Look for parasitized red blood cells.
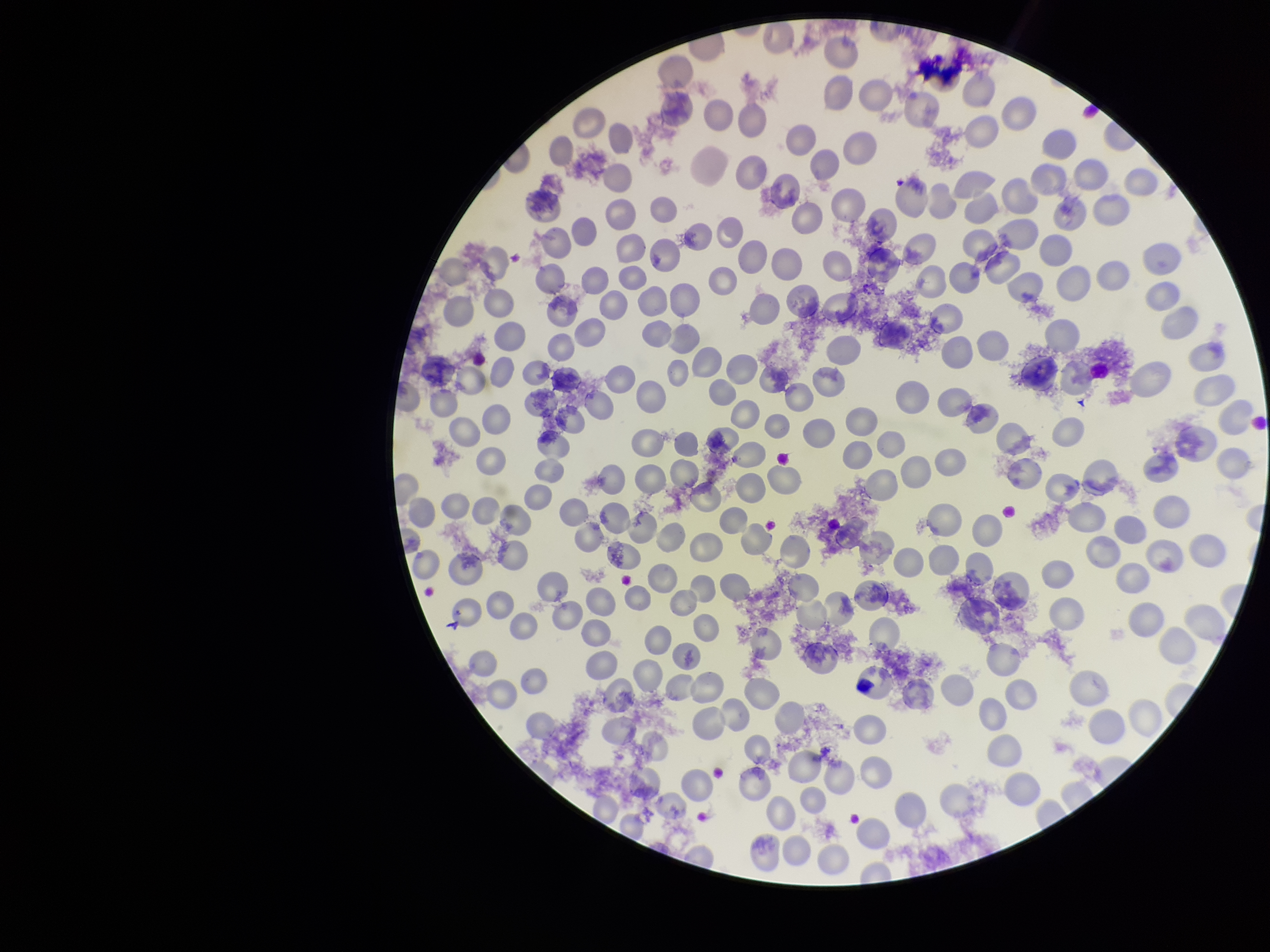
None seen.

One field from this slide. Preparation: thin. Parasitized red blood cell count: 0. Stained with Giemsa. Red blood cell count: 260. Species reported for this patient: Plasmodium falciparum. Image is 1270×952 pixels. Patient malaria status: infected. Photographed through the microscope eyepiece with a smartphone camera.